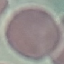
{
  "malaria_status": "uninfected",
  "image_type": "automatically extracted cell patch, resized to 64 × 64 pixels",
  "stain": "Giemsa",
  "capture": "smartphone through the microscope eyepiece",
  "preparation": "thin smear"
}